Give the position of every leukocyte visible.
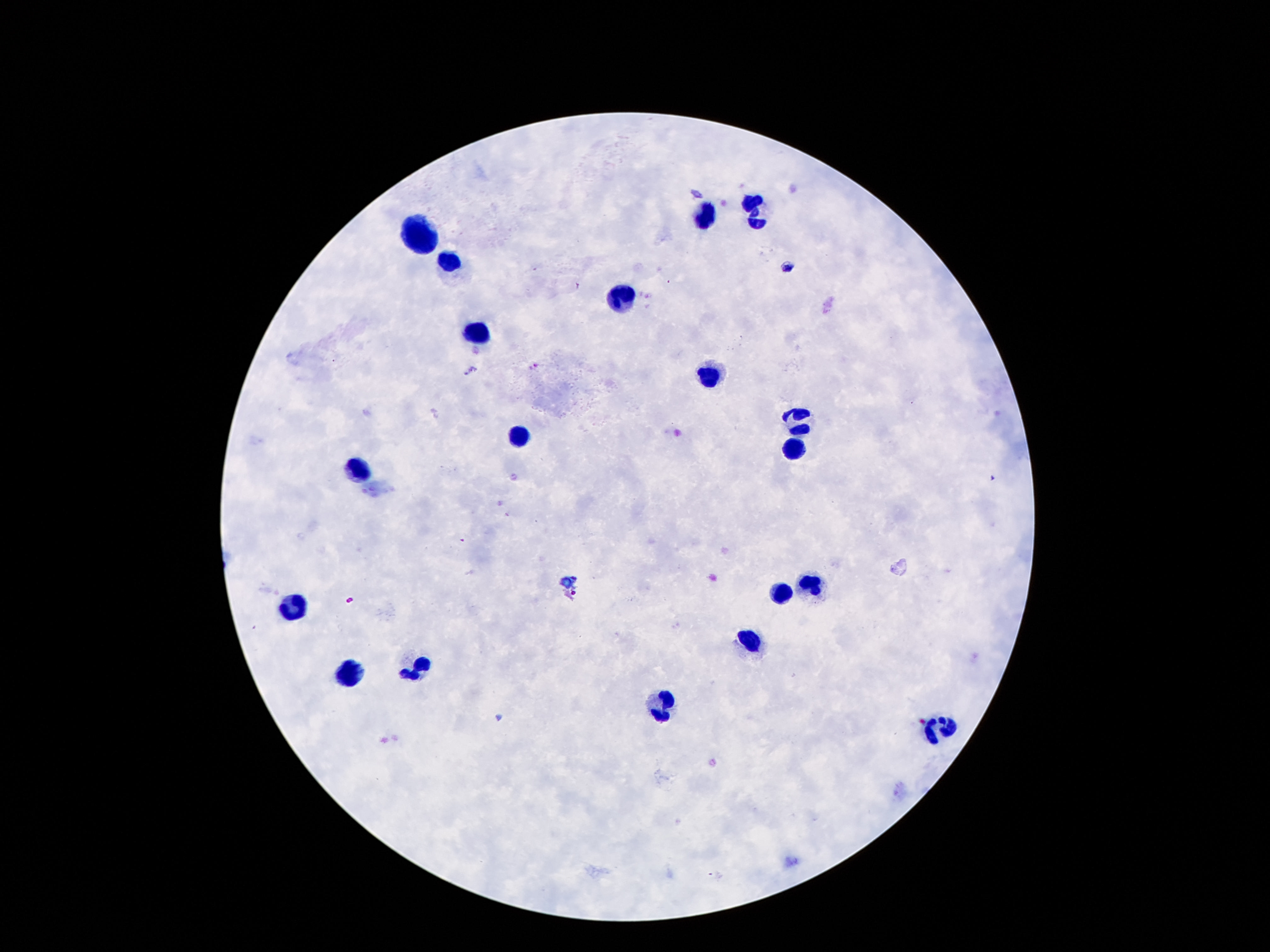
Approximate centers as [x, y] in pixels.
Leukocytes: [751, 209], [706, 215], [421, 231], [451, 263], [622, 301], [481, 334], [711, 374], [799, 420], [521, 438], [793, 449], [362, 474], [819, 584], [782, 594], [293, 607], [751, 639], [417, 668], [352, 674], [661, 698], [936, 732].

stain = Giemsa
capture = smartphone camera through the microscope eyepiece
preparation = thick blood smear
field of view = single
image size = 1270×952 pixels
magnification = 100x
patient malaria status = uninfected